Name the blood parasite species.
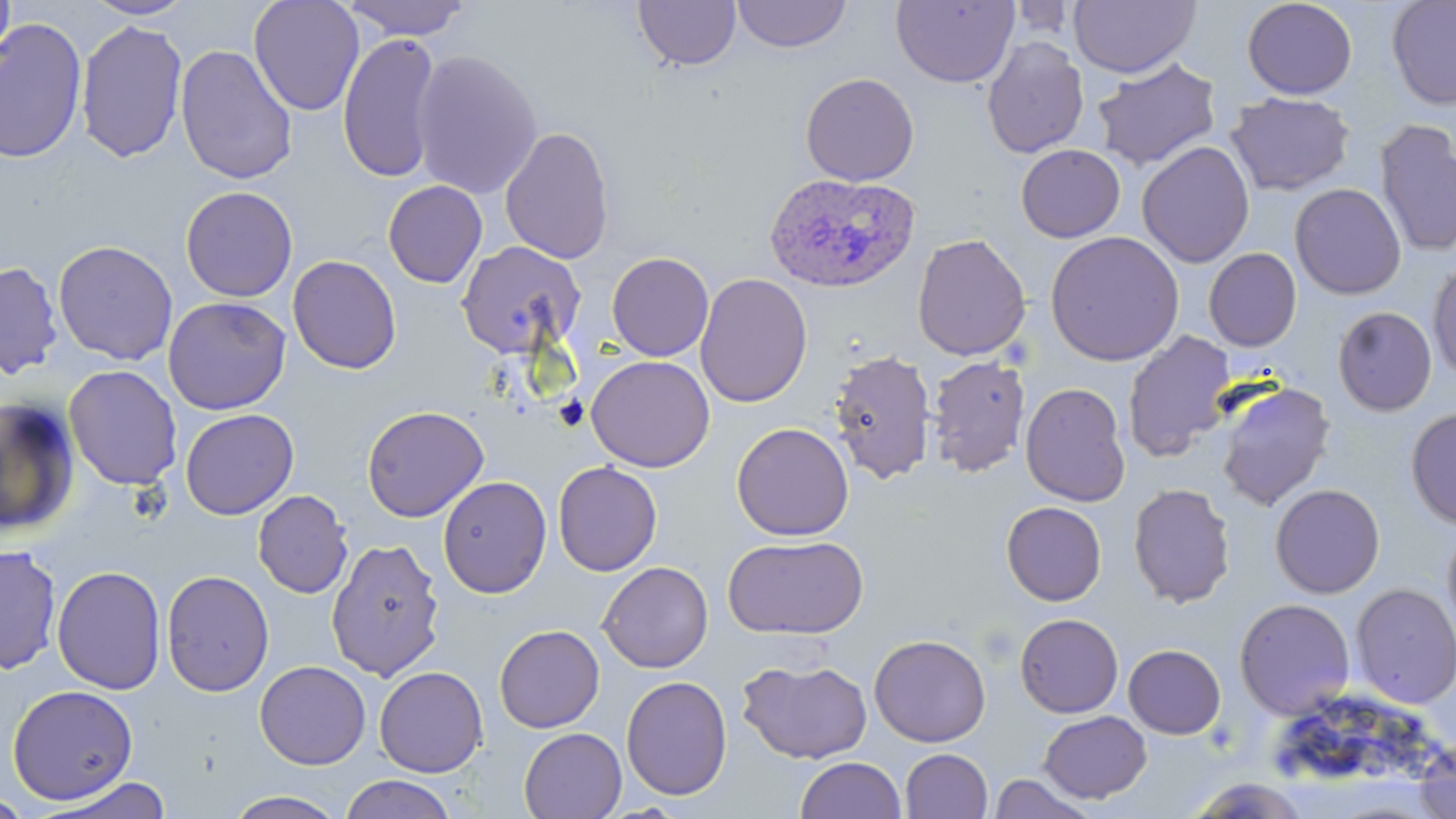

Plasmodium ovale.

Summary:
  - Coordinate format: approximate bounding boxes as [x1, y1, x2, y2] in pixels
  - Uninfected red blood cell locations: [0, 0, 16, 77], [81, 0, 196, 21], [248, 0, 365, 116], [341, 0, 471, 40], [891, 0, 1019, 88], [1069, 0, 1201, 79], [1241, 0, 1358, 100], [1386, 0, 1456, 110], [633, 1, 741, 71], [731, 1, 852, 53], [0, 17, 87, 165], [75, 19, 189, 164], [337, 33, 443, 183], [981, 36, 1089, 159], [175, 44, 298, 185], [410, 49, 543, 200], [1091, 58, 1222, 172], [800, 72, 920, 186], [1226, 91, 1355, 196], [1374, 119, 1456, 258], [499, 126, 616, 264], [1137, 141, 1255, 268], [1016, 144, 1125, 243], [382, 180, 488, 288], [1290, 182, 1407, 300], [179, 186, 298, 302], [1045, 231, 1184, 366], [912, 233, 1031, 361], [52, 240, 178, 366], [456, 240, 587, 359], [1203, 248, 1302, 351], [606, 251, 714, 361], [287, 255, 402, 375], [1427, 259, 1456, 382], [0, 261, 63, 379], [695, 272, 813, 408], [163, 296, 291, 415], [1332, 306, 1437, 416], [1122, 330, 1237, 462], [828, 348, 937, 485], [585, 355, 716, 472], [925, 355, 1031, 479], [64, 365, 183, 490], [1214, 381, 1336, 512], [1020, 382, 1131, 506], [0, 396, 80, 536], [361, 405, 489, 522], [1405, 407, 1456, 529], [179, 408, 299, 520], [731, 422, 854, 541], [552, 462, 663, 576], [437, 475, 552, 599], [1127, 482, 1236, 609], [1269, 484, 1385, 598], [252, 490, 353, 599], [1001, 501, 1107, 605], [1442, 523, 1456, 642], [722, 535, 869, 640], [326, 537, 446, 681], [1, 544, 62, 676], [597, 561, 713, 673], [51, 565, 167, 694], [161, 570, 274, 697], [1350, 583, 1456, 708], [1233, 598, 1356, 720], [1015, 613, 1124, 718], [494, 624, 605, 733], [868, 633, 992, 748], [1123, 644, 1226, 739], [737, 658, 873, 764], [254, 660, 371, 770], [374, 666, 489, 777], [620, 675, 732, 800], [6, 684, 138, 805], [1038, 710, 1152, 804], [518, 727, 627, 818], [1414, 738, 1456, 819], [900, 748, 993, 819], [795, 756, 906, 819], [987, 772, 1098, 818], [340, 774, 457, 819], [39, 776, 173, 818], [1184, 776, 1314, 817], [222, 790, 350, 818], [0, 793, 34, 818]
  - Plasmodium ovale-infected red blood cell locations: [764, 172, 920, 294]
  - Stain: May-Grünwald-Giemsa
  - Image size: 1456×819 pixels
  - Magnification: 1000x
  - Field of view: one of a larger specimen
  - Preparation: thin blood smear
  - Modality: light microscopy